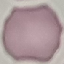
Result: negative for malaria parasites. Giemsa stain. Photographed with a smartphone camera at the microscope eyepiece. Automatically extracted cell patch, resized to 64 × 64 pixels. Thin blood film.